Outline each blood parasite and name the species.
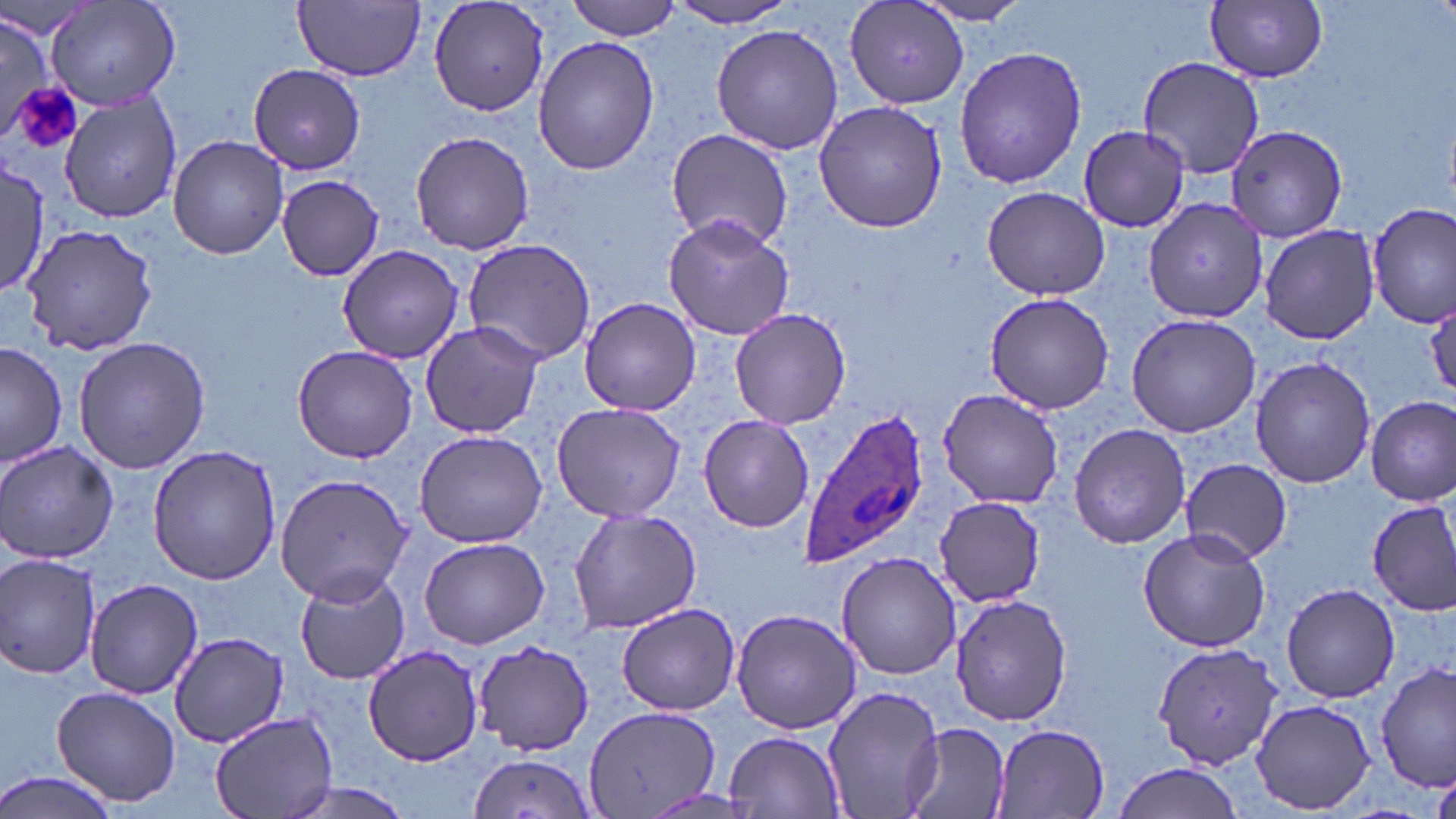

Approximate bounding boxes as (x1, y1, x2, y2) in pixels.
Plasmodium ovale-infected red blood cells: (797, 404, 933, 570).
No Plasmodium falciparum, Plasmodium malariae, Plasmodium vivax, Babesia divergens, or Trypanosoma brucei observed.

slide_level_diagnosis: Plasmodium ovale
stain: May-Grünwald-Giemsa
modality: light microscopy
image_size: 1456×819 pixels
field_of_view: one of a larger specimen
magnification: 1000x
uninfected_red_blood_cell_locations: 'approximate bounding boxes as (x1, y1, x2, y2) in pixels: (45, 0, 183, 110), (294, 0, 425, 80), (568, 0, 684, 41), (843, 0, 969, 110), (664, 1, 802, 28), (908, 1, 1035, 26), (1206, 1, 1328, 83), (427, 2, 551, 117), (0, 18, 57, 136), (710, 23, 843, 156), (533, 36, 660, 176), (953, 46, 1088, 191), (1137, 56, 1265, 179), (249, 65, 365, 173), (59, 95, 182, 222), (813, 99, 948, 233), (1227, 123, 1348, 243), (1078, 124, 1190, 234), (666, 129, 795, 250), (411, 131, 534, 255), (168, 135, 289, 259), (1, 159, 50, 299), (276, 174, 385, 280), (981, 185, 1114, 300), (1141, 198, 1268, 321), (1368, 204, 1454, 329), (664, 214, 794, 341), (23, 222, 159, 356), (1258, 223, 1382, 345), (462, 239, 595, 365), (337, 245, 465, 363), (984, 291, 1114, 414), (579, 295, 700, 417), (729, 307, 851, 429), (1126, 313, 1260, 437), (420, 319, 547, 441), (71, 335, 212, 473), (1, 342, 69, 468), (291, 344, 418, 462), (1249, 356, 1376, 489), (938, 390, 1063, 509), (1366, 396, 1455, 506), (552, 402, 686, 523), (698, 413, 814, 532), (1067, 424, 1191, 548), (414, 429, 550, 548), (0, 440, 120, 566), (148, 445, 281, 585), (1181, 459, 1292, 563), (275, 473, 412, 605), (931, 497, 1046, 606), (1369, 501, 1456, 616), (568, 507, 702, 635), (1136, 526, 1272, 654), (418, 537, 550, 649), (836, 551, 961, 680), (0, 555, 102, 680), (294, 571, 410, 684), (84, 578, 203, 698), (1281, 581, 1400, 703), (950, 593, 1073, 725), (615, 603, 741, 716), (731, 608, 860, 735), (170, 631, 289, 750), (476, 643, 594, 754), (1154, 643, 1281, 769), (363, 645, 483, 766), (1375, 662, 1453, 792), (51, 683, 182, 808), (820, 685, 946, 819), (1250, 698, 1376, 815), (582, 705, 721, 819), (209, 712, 338, 819), (901, 722, 1010, 819), (990, 723, 1111, 817), (725, 730, 845, 816), (464, 754, 598, 819), (1111, 763, 1246, 817), (0, 770, 121, 819), (1430, 774, 1456, 819)'
preparation: thin blood smear
platelet_locations: 'approximate bounding boxes as (x1, y1, x2, y2) in pixels: (11, 83, 83, 156)'